Classify this cell by malaria status.
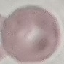

It is uninfected.

Summary:
  - Stain: Giemsa
  - Preparation: thin smear
  - Capture: smartphone through the microscope eyepiece
  - Image type: cell patch, automatically extracted from a larger field of view and resized to 64 × 64 pixels